Assess the morphology of the red blood cells.
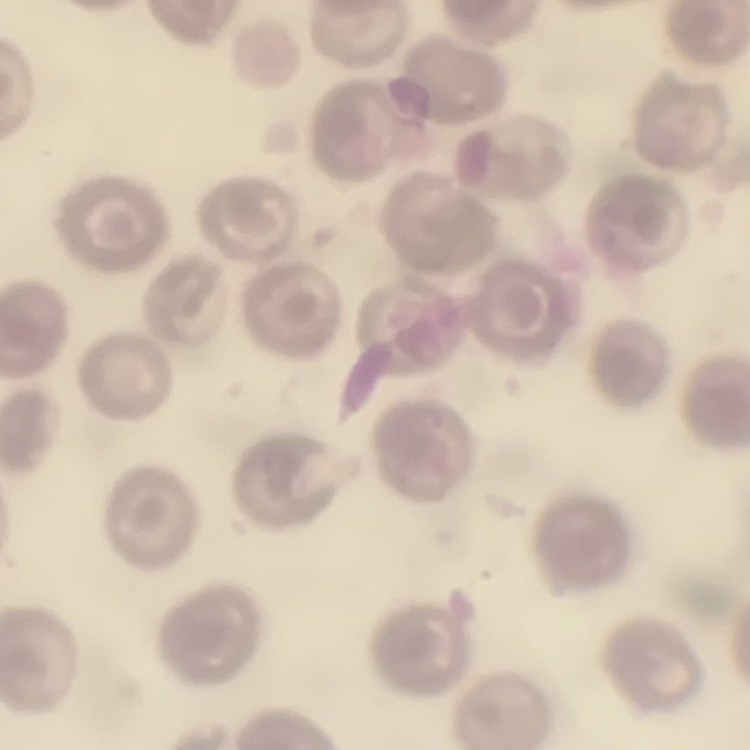
They show no rouleaux formation.

Field's or Giemsa stain. Thin blood smear. Square crop of a larger photomicrograph.